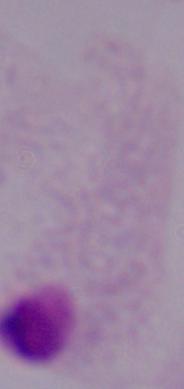

Micrograph. A trichomonad is seen. Captured at 1000x magnification.